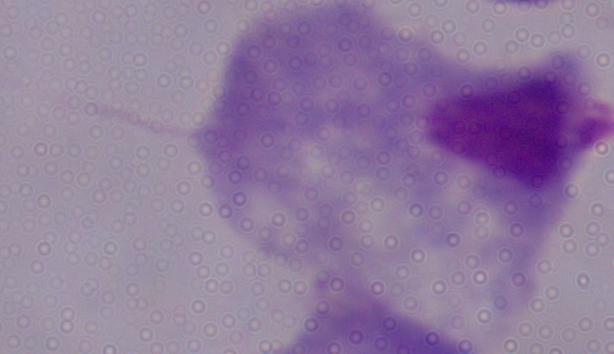
Summary:
  - Identification: trichomonad
  - Modality: micrograph
  - Magnification: 1000x